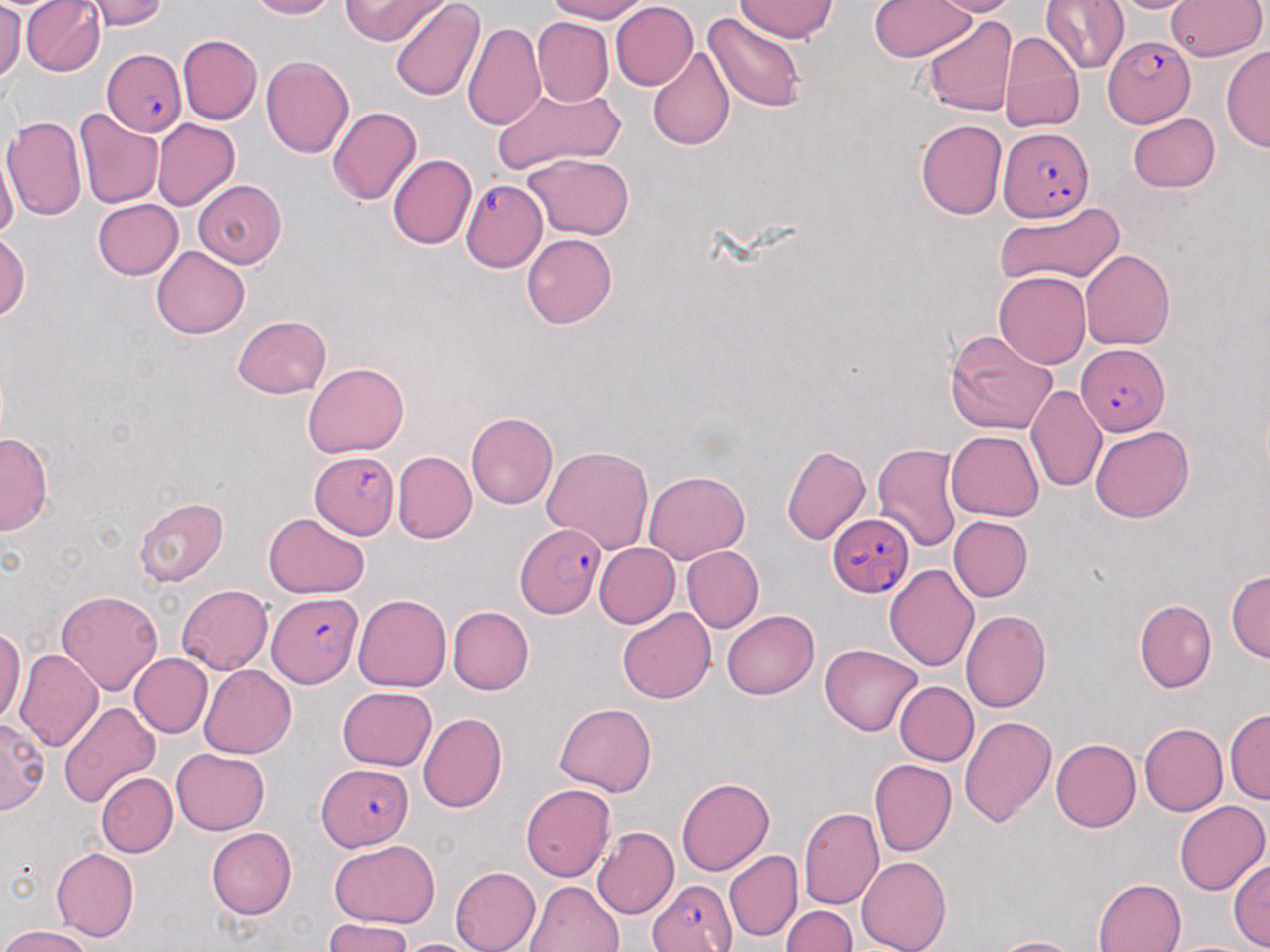

slide-level diagnosis = Plasmodium falciparum
modality = light microscopy
field of view = one of a larger specimen
stain = May-Grünwald-Giemsa
Plasmodium falciparum-infected red blood cell locations = approximate bounding boxes as (x1, y1, x2, y2) in pixels: (1102, 36, 1194, 127), (100, 50, 185, 133), (1002, 128, 1092, 220), (459, 181, 546, 272), (1074, 343, 1168, 436), (309, 452, 400, 540), (828, 513, 913, 598), (514, 521, 608, 616), (266, 591, 364, 687), (316, 765, 415, 851), (644, 878, 737, 952)
magnification = 1000x
image size = 1270×952 pixels
preparation = thin blood smear
uninfected red blood cell locations = approximate bounding boxes as (x1, y1, x2, y2) in pixels: (0, 0, 21, 86), (21, 0, 104, 76), (89, 0, 167, 30), (241, 0, 345, 20), (340, 0, 442, 46), (539, 0, 655, 22), (737, 0, 835, 43), (868, 0, 980, 62), (925, 0, 1024, 15), (1042, 0, 1129, 74), (1110, 0, 1197, 15), (1169, 0, 1266, 63), (388, 2, 483, 103), (611, 3, 698, 91), (705, 10, 805, 113), (923, 14, 1018, 116), (533, 19, 614, 104), (462, 21, 545, 132), (1001, 29, 1083, 132), (178, 33, 262, 123), (646, 45, 735, 151), (1223, 45, 1270, 155), (262, 54, 355, 161), (488, 82, 626, 176), (76, 106, 162, 209), (328, 106, 420, 208), (1127, 112, 1222, 192), (4, 114, 88, 222), (915, 118, 1007, 221), (152, 121, 238, 211), (522, 152, 635, 239), (389, 154, 477, 250), (0, 156, 16, 247), (196, 180, 291, 269), (91, 199, 181, 280), (995, 201, 1123, 290), (0, 231, 29, 331), (523, 234, 617, 329), (151, 246, 247, 338), (1080, 251, 1175, 348), (993, 269, 1090, 366), (230, 314, 331, 399), (944, 330, 1058, 437), (302, 361, 408, 460), (1029, 384, 1107, 497), (466, 412, 558, 510), (1088, 425, 1194, 521), (946, 430, 1044, 522), (1, 431, 51, 535), (780, 443, 871, 546), (873, 443, 964, 554), (542, 445, 653, 555), (391, 451, 476, 546), (642, 470, 750, 562), (135, 495, 230, 587), (263, 513, 368, 597), (949, 516, 1032, 603), (595, 543, 678, 627), (680, 546, 763, 634), (884, 563, 979, 673), (1227, 568, 1269, 665), (176, 584, 272, 675), (58, 588, 163, 693), (354, 594, 451, 690), (1135, 599, 1215, 691), (447, 607, 534, 693), (617, 608, 716, 705), (722, 610, 819, 699), (962, 610, 1051, 714), (0, 622, 24, 728), (820, 643, 924, 737), (14, 648, 101, 752), (128, 653, 211, 739), (199, 665, 296, 758), (894, 681, 978, 766), (337, 686, 437, 772), (59, 700, 160, 811), (552, 702, 658, 797), (1226, 710, 1269, 807), (417, 712, 508, 811), (960, 713, 1058, 830), (2, 716, 47, 814), (1138, 722, 1227, 816), (1052, 738, 1141, 832), (170, 749, 271, 835), (869, 757, 955, 856), (95, 772, 176, 858), (675, 775, 774, 874), (522, 784, 613, 880), (1174, 799, 1270, 896), (799, 808, 884, 909), (593, 826, 678, 918), (207, 829, 297, 917), (328, 841, 440, 927), (50, 847, 140, 941), (725, 851, 800, 941), (855, 856, 951, 951), (1229, 856, 1270, 949), (451, 868, 541, 952), (1093, 876, 1183, 952), (527, 880, 624, 952), (781, 903, 858, 952), (321, 918, 414, 952), (0, 925, 94, 952), (990, 934, 1083, 952), (1170, 936, 1259, 952), (398, 937, 482, 952)